Report the malaria status of this cell.
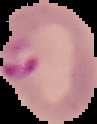

It is parasitized.

Summary:
  - Preparation: thin blood film
  - Image size: 97×124 pixels
  - Image type: cell region segmented out of the field of view; surrounding area masked to black